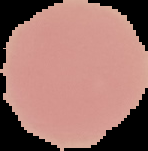
Segmented cell region on a black background. Result: no malaria parasites seen. From a thin blood smear. Image is 148×151 pixels.